Describe the morphology of the erythrocytes.
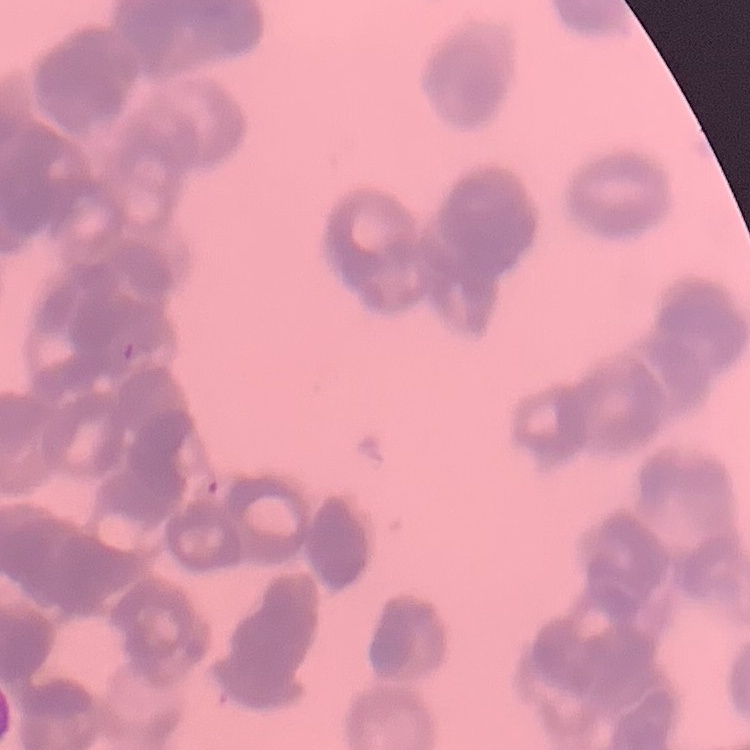

Rouleaux formation.

image type = square crop of a larger photomicrograph
stain = Field's or Giemsa
preparation = thin peripheral smear